Point out each malaria parasite.
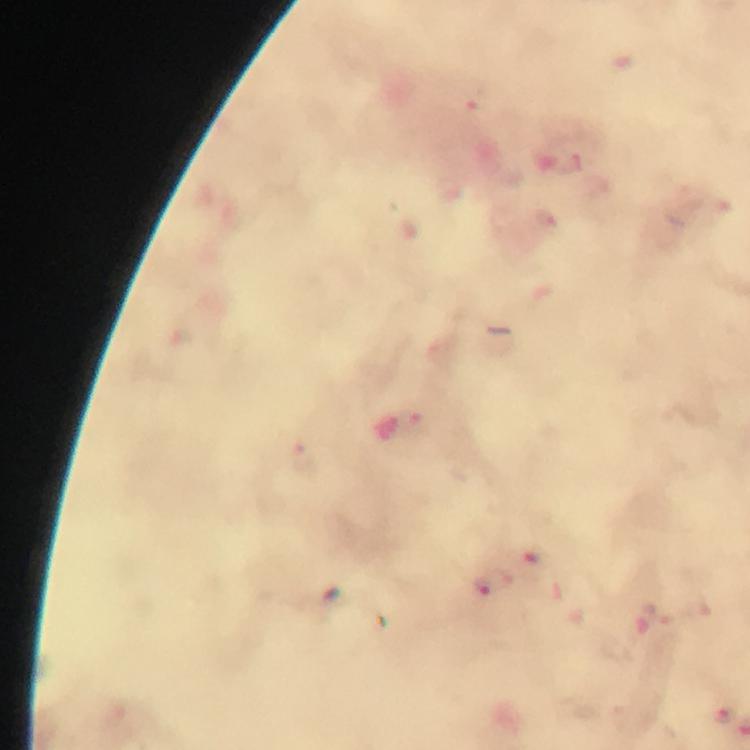
Approximate centers as (x, y) in pixels.
Malaria parasites: (468, 98), (573, 162), (301, 456), (503, 581), (482, 584), (721, 713).

Summary:
  - Preparation: thick blood film
  - Magnification: 100x
  - Capture: smartphone mounted on the microscope
  - Cropped from: one field of view
  - Context: from a diagnostic examination for malaria
  - Image size: 750×750 pixels
  - Immersion oil: applied
  - Stain: Giemsa